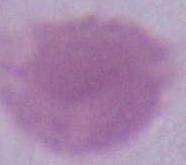

Captured at 1000x magnification. Micrograph. A red blood cell is seen.